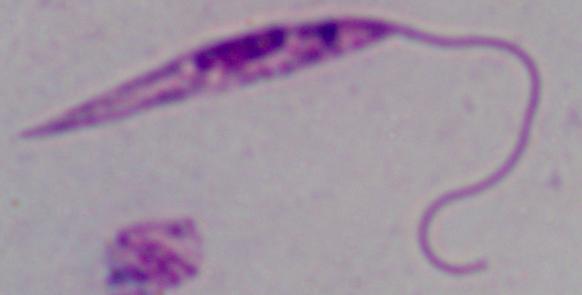
Summary:
  - Modality: photomicrograph
  - Identification: Leishmania
  - Magnification: 1000x